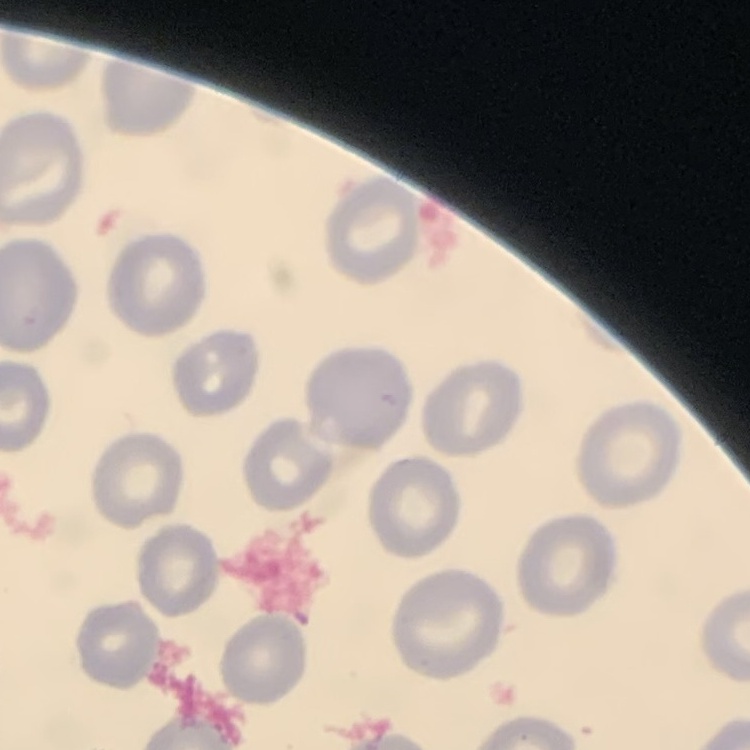
The erythrocytes show no rouleaux formation. Stained with either Field's or Giemsa. Thin blood film. One tile cut from a larger photomicrograph.